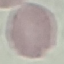
Result: no malaria parasites seen. Acquired by smartphone through the microscope eyepiece. Cell patch, automatically extracted from a larger field of view and resized to 64 × 64 pixels. Thin smear of blood. Giemsa-stained preparation.